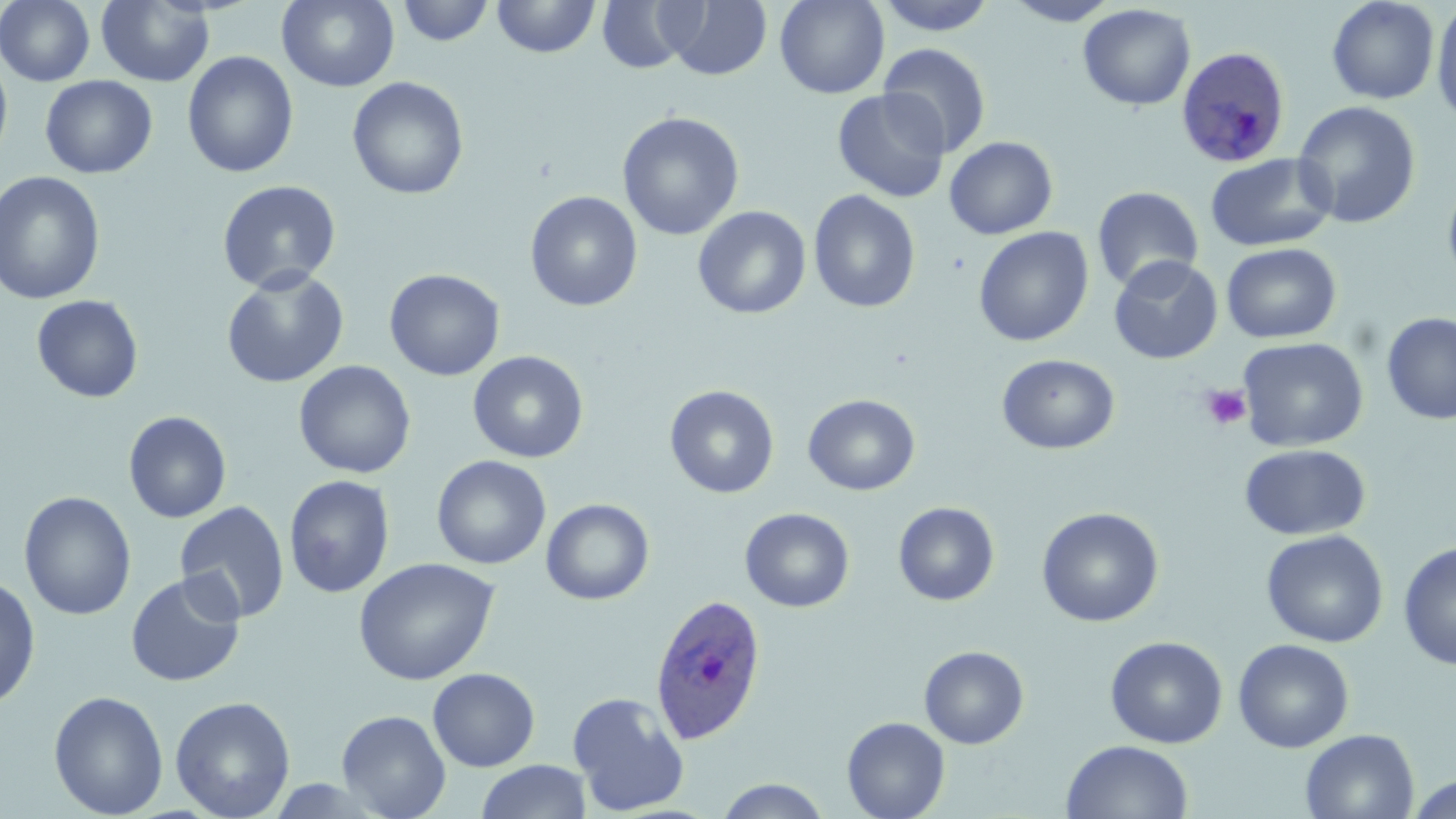

Summary:
  - Coordinate format: approximate bounding boxes as [x1, y1, x2, y2] in pixels
  - Plasmodium ovale-infected red blood cell locations: [1172, 47, 1287, 169], [649, 593, 768, 746]
  - Platelet locations: [1200, 385, 1253, 432]
  - Uninfected red blood cell locations: [0, 0, 95, 87], [277, 0, 400, 91], [492, 0, 600, 58], [597, 0, 697, 73], [775, 0, 889, 99], [874, 0, 999, 35], [1004, 0, 1119, 26], [1326, 0, 1439, 104], [1430, 0, 1456, 128], [96, 1, 215, 87], [397, 1, 494, 46], [663, 1, 772, 80], [1077, 3, 1196, 111], [878, 43, 992, 157], [182, 51, 299, 178], [0, 53, 14, 170], [40, 75, 157, 178], [347, 76, 469, 200], [832, 88, 951, 203], [1293, 101, 1421, 229], [616, 111, 745, 241], [943, 136, 1059, 240], [1204, 154, 1336, 252], [0, 170, 106, 306], [1442, 174, 1456, 292], [217, 180, 341, 294], [1091, 186, 1203, 292], [524, 190, 643, 312], [808, 190, 921, 313], [692, 205, 811, 319], [973, 226, 1094, 347], [1221, 242, 1341, 343], [1108, 255, 1224, 364], [221, 267, 350, 389], [383, 268, 505, 381], [31, 295, 144, 403], [1381, 312, 1456, 425], [1238, 336, 1369, 452], [468, 350, 589, 463], [996, 354, 1120, 455], [293, 360, 416, 479], [664, 385, 780, 499], [802, 394, 920, 496], [123, 411, 232, 523], [1239, 443, 1371, 541], [431, 455, 551, 570], [283, 475, 395, 598], [18, 490, 137, 620], [541, 498, 654, 605], [174, 501, 290, 624], [893, 501, 1000, 606], [739, 507, 855, 613], [1036, 507, 1164, 627], [1260, 529, 1389, 648], [1398, 541, 1456, 671], [353, 557, 499, 686], [124, 571, 246, 688], [0, 574, 41, 710], [1105, 635, 1228, 748], [1233, 638, 1354, 753], [919, 645, 1029, 749], [427, 668, 540, 771], [48, 690, 168, 818], [568, 692, 690, 816], [170, 696, 296, 819], [337, 709, 451, 819], [842, 716, 950, 819], [1300, 729, 1419, 818], [1060, 740, 1194, 819], [476, 760, 592, 819], [714, 777, 832, 818], [1406, 777, 1454, 819]
  - Slide-level diagnosis: Plasmodium ovale
  - Modality: optical microscopy
  - Magnification: 1000x
  - Stain: May-Grünwald-Giemsa
  - Field of view: one of a larger specimen
  - Image size: 1456×819 pixels
  - Preparation: thin blood smear